Identify the parasite.
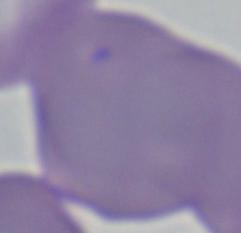
This is Babesia.

1000x magnification. Photomicrograph.